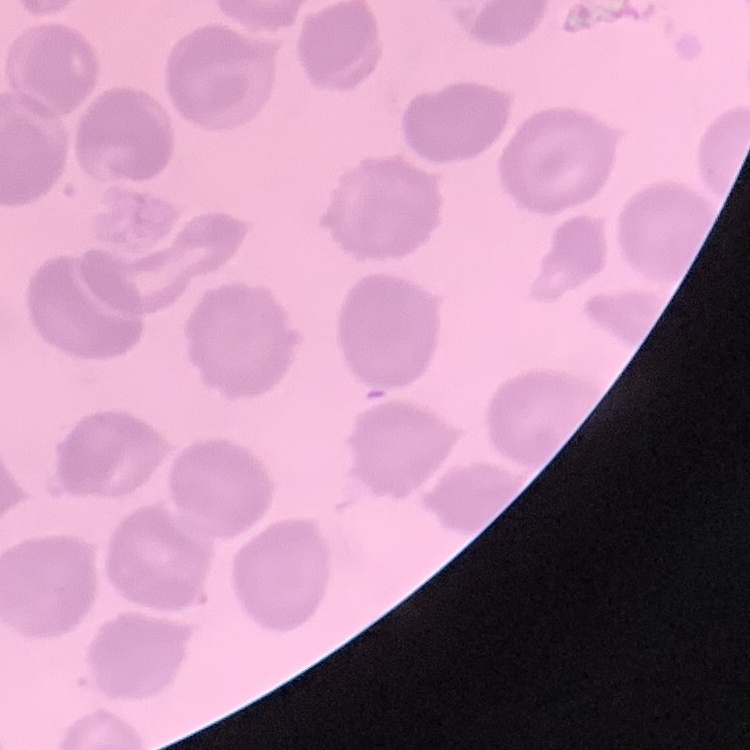

The red blood cells show no rouleaux formation. Thin blood film. Field's or Giemsa stain. Square crop of a larger photomicrograph.